Describe the morphology of the erythrocytes.
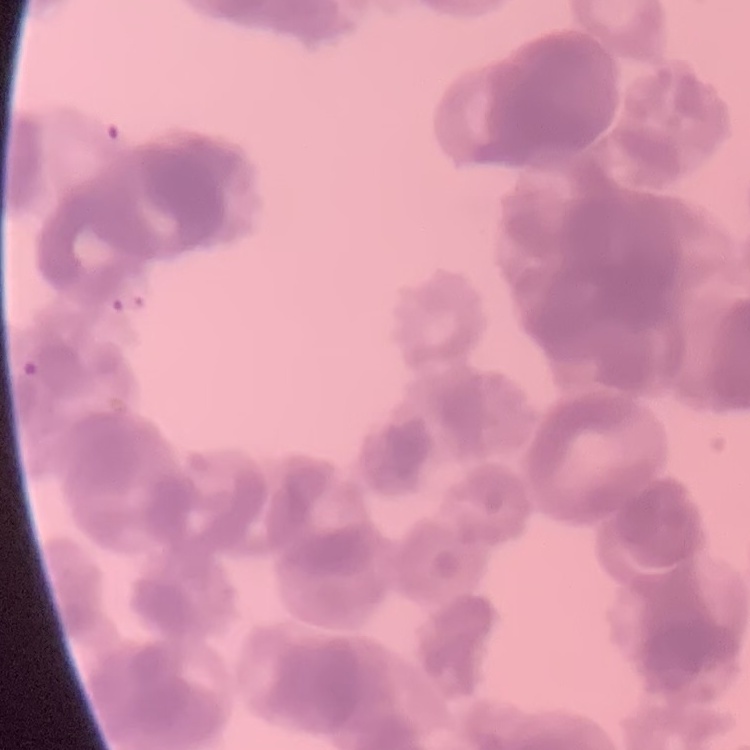

Rouleaux formation.

image type = square crop of a larger photomicrograph
stain = Field's or Giemsa
preparation = thin blood film